Give the extent of all Plasmodium ovale-infected red blood cells.
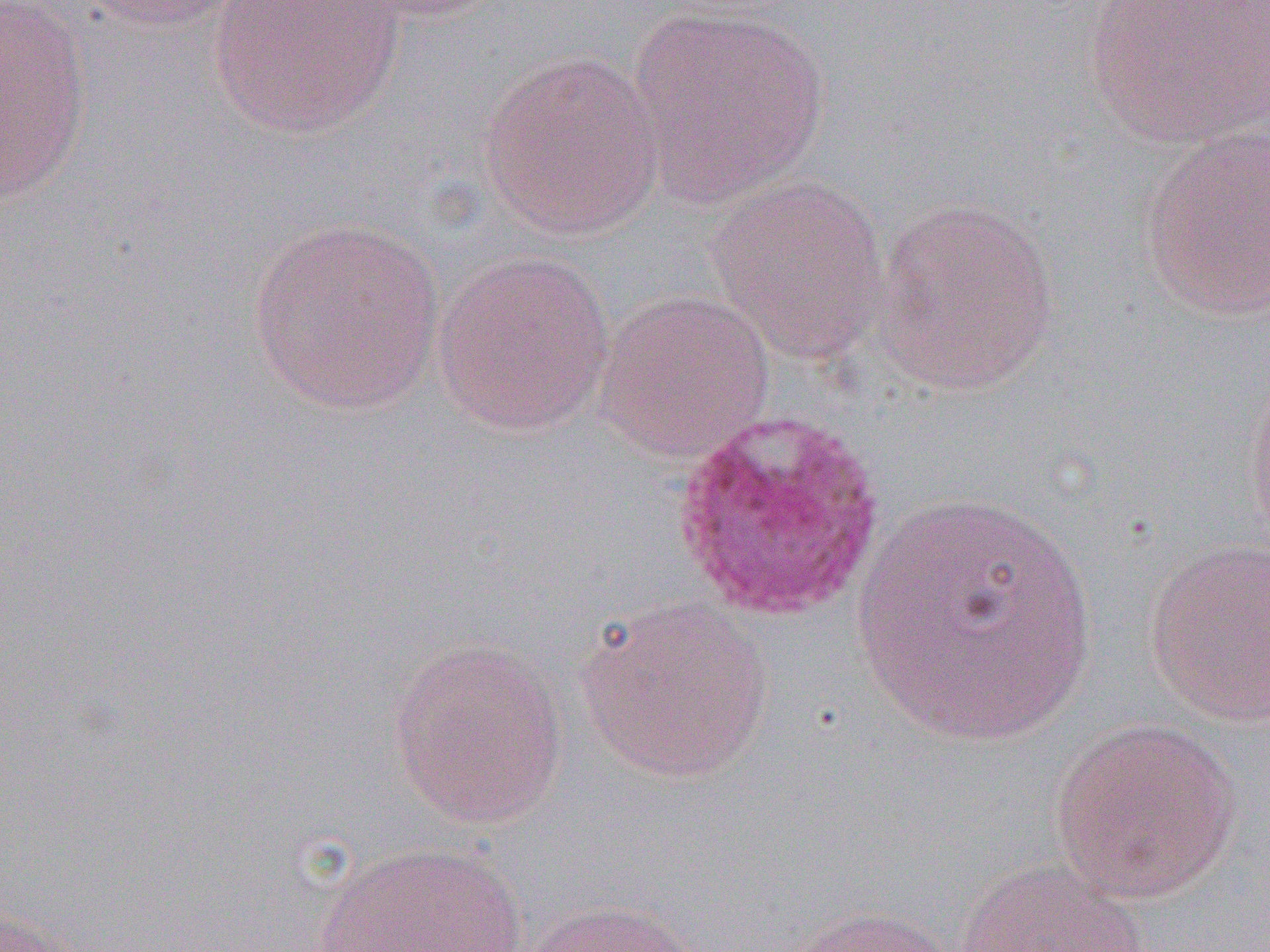

Approximate bounding boxes as (x1, y1, x2, y2) in pixels.
Plasmodium ovale-infected red blood cells: (669, 409, 888, 623).

{
  "slide_level_diagnosis": "Plasmodium ovale",
  "uninfected_red_blood_cell_locations": "approximate bounding boxes as (x1, y1, x2, y2) in pixels: (0, 0, 94, 207), (74, 0, 255, 31), (209, 0, 405, 140), (335, 0, 507, 24), (1087, 0, 1270, 150), (625, 4, 830, 209), (478, 49, 667, 243), (1140, 122, 1270, 322), (704, 173, 892, 365), (870, 198, 1061, 397), (246, 216, 446, 416), (431, 249, 616, 437), (593, 290, 775, 463), (1242, 373, 1270, 556), (850, 490, 1098, 745), (1144, 537, 1270, 726), (575, 596, 774, 785), (388, 637, 568, 830), (1049, 716, 1243, 904), (310, 839, 537, 952), (953, 856, 1152, 952), (521, 898, 706, 952), (782, 905, 961, 952), (0, 908, 82, 952)",
  "modality": "optical microscopy",
  "image_size": "1270×952 pixels",
  "magnification": "1000x",
  "field_of_view": "one of a larger specimen",
  "preparation": "thin blood smear"
}